Evaluate for malaria.
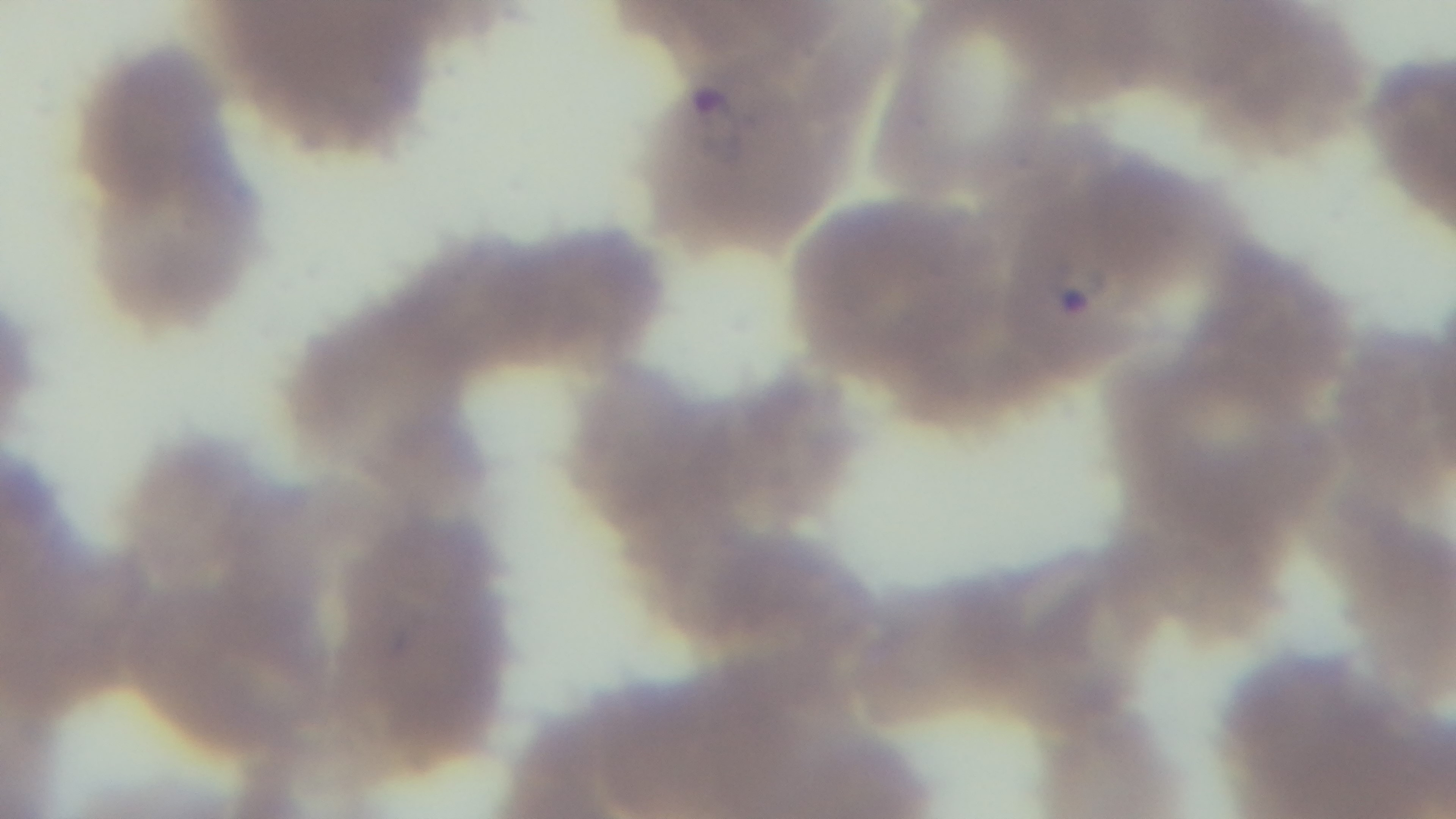
Positive.

stain = Giemsa
field of view = single
preparation = thin blood film
capture = mounted 4K digital camera
objective = 100x oil immersion
modality = light microscopy